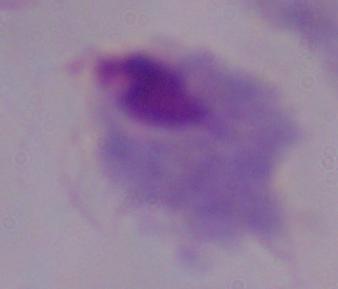

1000x magnification. A trichomonad is seen. Photomicrograph.